Give the preparation type.
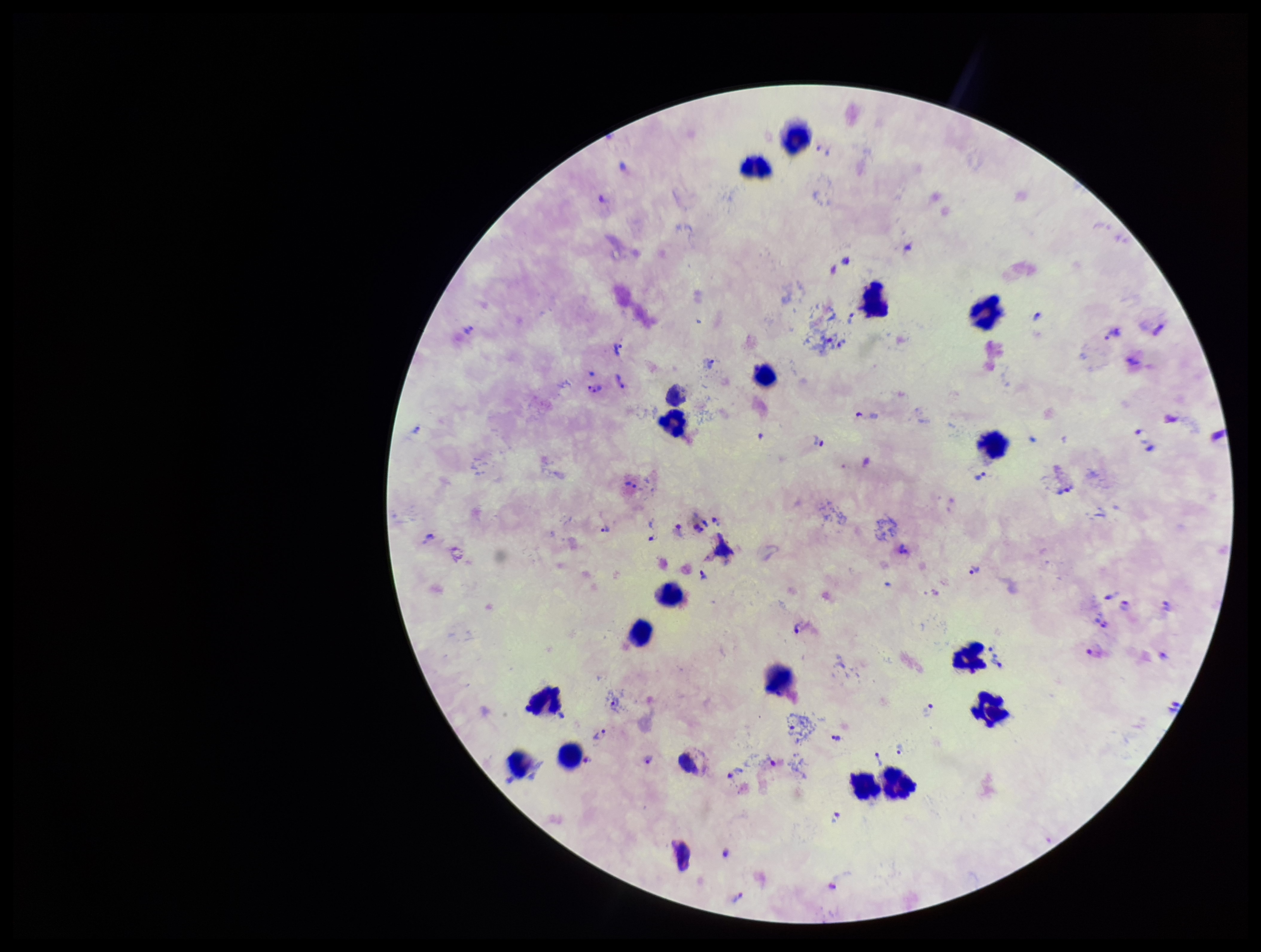

It is a thick blood smear.

patient malaria status = positive
capture = smartphone photograph through the microscope eyepiece
parasite count = 47
Plasmodium parasites = identified
leukocyte count = 17
image size = 1261×952 pixels
species reported for this patient = Plasmodium vivax
stain = Giemsa
field of view = one from this slide